State the preparation type.
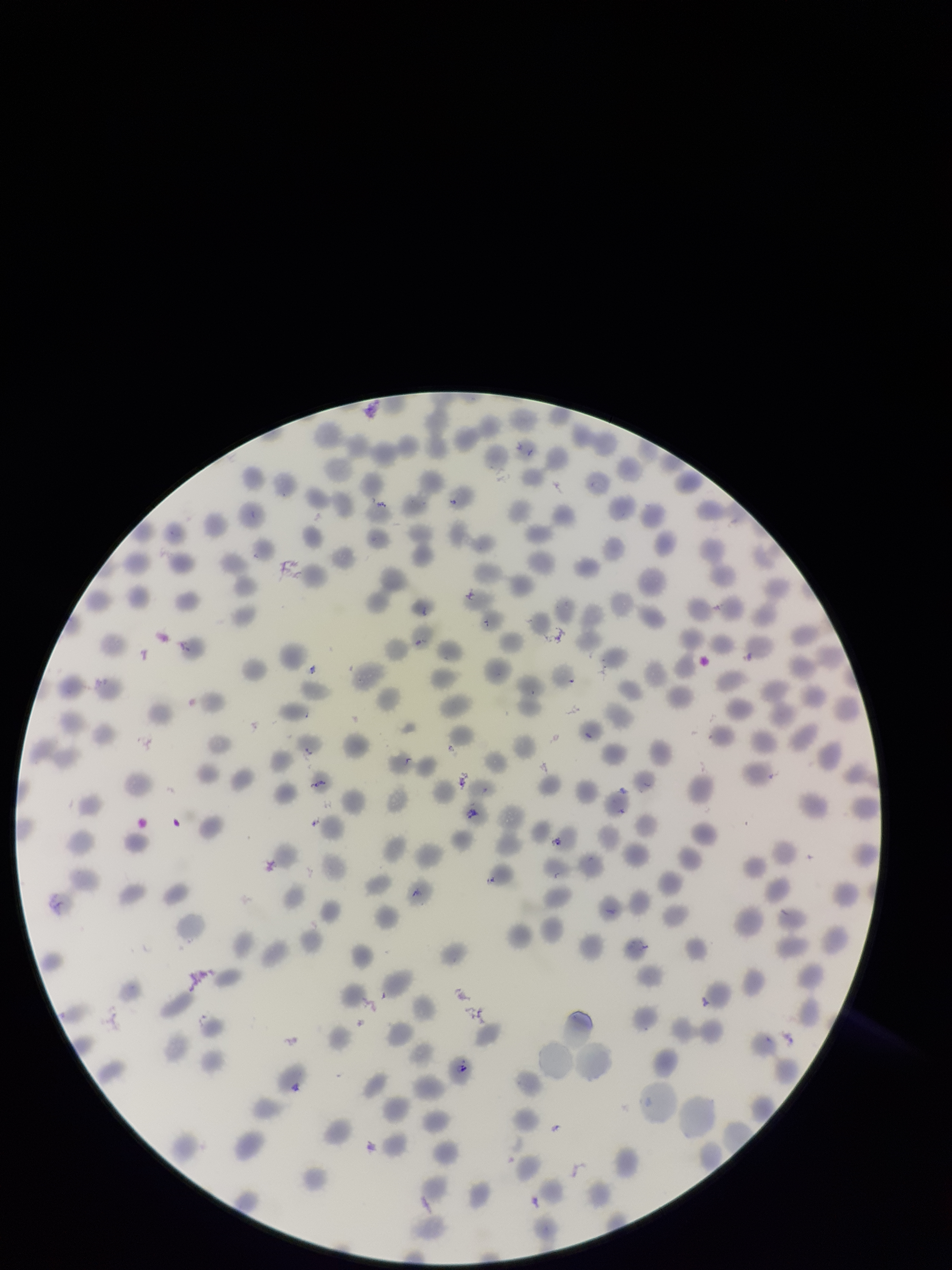
Thin.

{
  "stain": "Giemsa",
  "red_blood_cell_count": 246,
  "species_reported_for_this_patient": "Plasmodium falciparum",
  "patient_malaria_status": "positive",
  "parasitized_red_blood_cell_count": 0,
  "field_of_view": "single",
  "image_size": "952×1270 pixels",
  "parasitized_red_blood_cells": "none identified",
  "capture": "smartphone photograph through the microscope eyepiece"
}